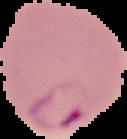

Summary:
  - Image type: cell region segmented out of the field of view; surrounding area masked to black
  - Preparation: thin blood film
  - Image size: 127×139 pixels
  - Malaria status: parasitized